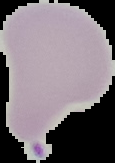

Summary:
  - Preparation: thin blood smear
  - Malaria status: uninfected
  - Image size: 115×163 pixels
  - Image type: segmented cell region on a black background